Assess this cell for malaria.
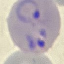
It is parasitized.

Giemsa stain. Photographed with a smartphone camera at the microscope eyepiece. Cell patch, automatically extracted from a larger field of view and resized to 64 × 64 pixels. Thin blood smear.